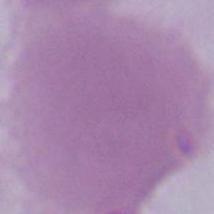
magnification: 1000x
modality: micrograph
identification: red blood cell